Evaluate for malaria.
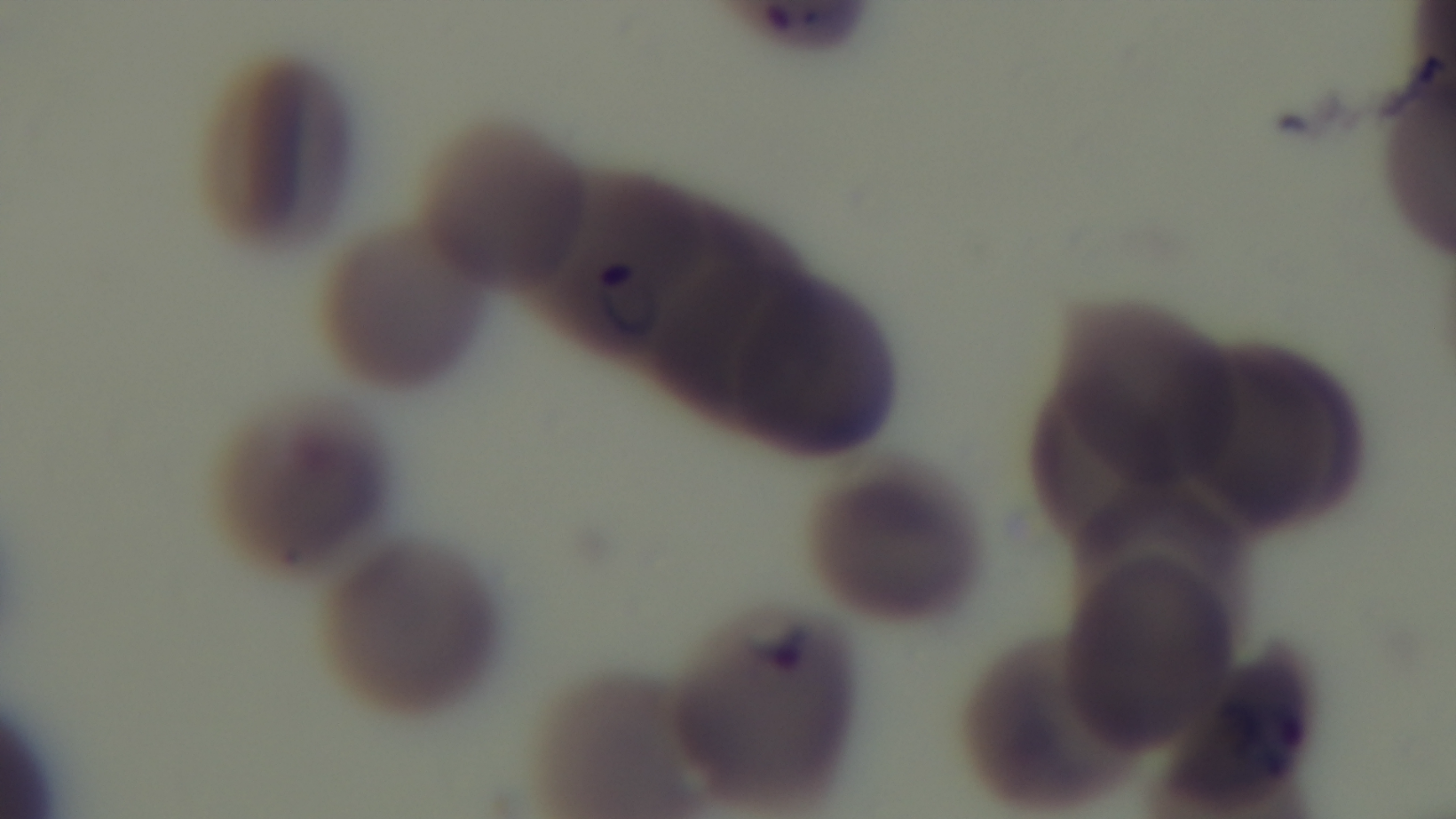
Positive.

Summary:
  - Stain: Giemsa
  - Objective: 100x oil immersion
  - Field of view: one from the slide
  - Modality: light microscopy
  - Preparation: thin
  - Capture: mounted 4K digital camera